Point out each leukocyte.
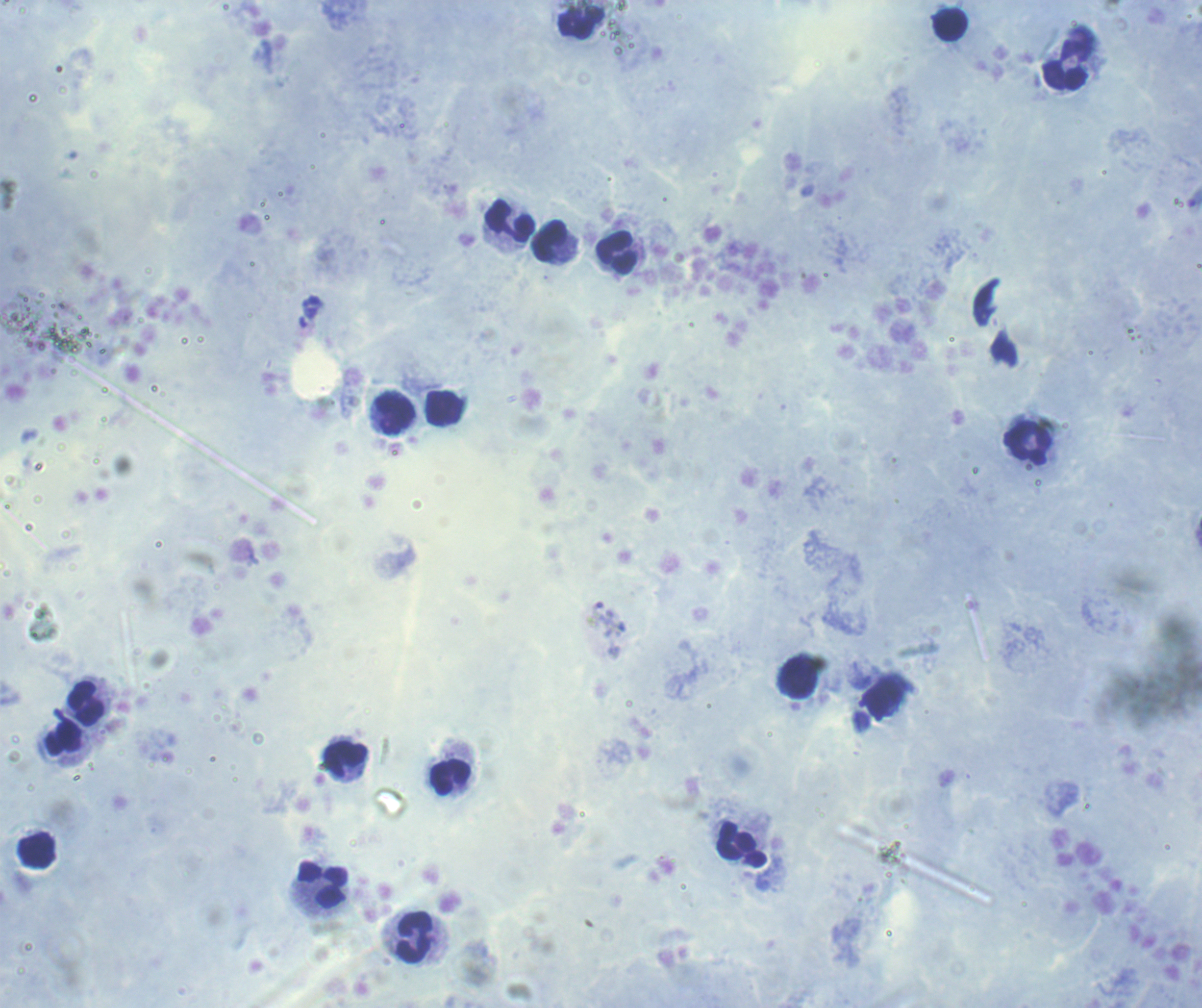
Approximate object centers, in pixels from the top-left corner.
Leukocytes: (x=582, y=23), (x=950, y=26), (x=1066, y=65), (x=510, y=220), (x=549, y=240), (x=616, y=252), (x=444, y=408), (x=395, y=414), (x=1028, y=444), (x=87, y=702), (x=64, y=739), (x=346, y=759), (x=449, y=777), (x=742, y=845), (x=322, y=885), (x=415, y=937).

Coloration quality: good. Previously used in an actual diagnosis. Thick blood smear. Result: no malaria parasites seen. Single field of view. Romanowsky stain. Image is 1202×1008 pixels. Background quality: good. 100x magnification.